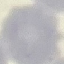

Malaria status: uninfected. Automatically extracted cell patch, resized to 64 × 64 pixels. Photographed with a smartphone camera at the microscope eyepiece. Giemsa-stained preparation. Thin blood film.